Locate every leukocyte (white blood cell).
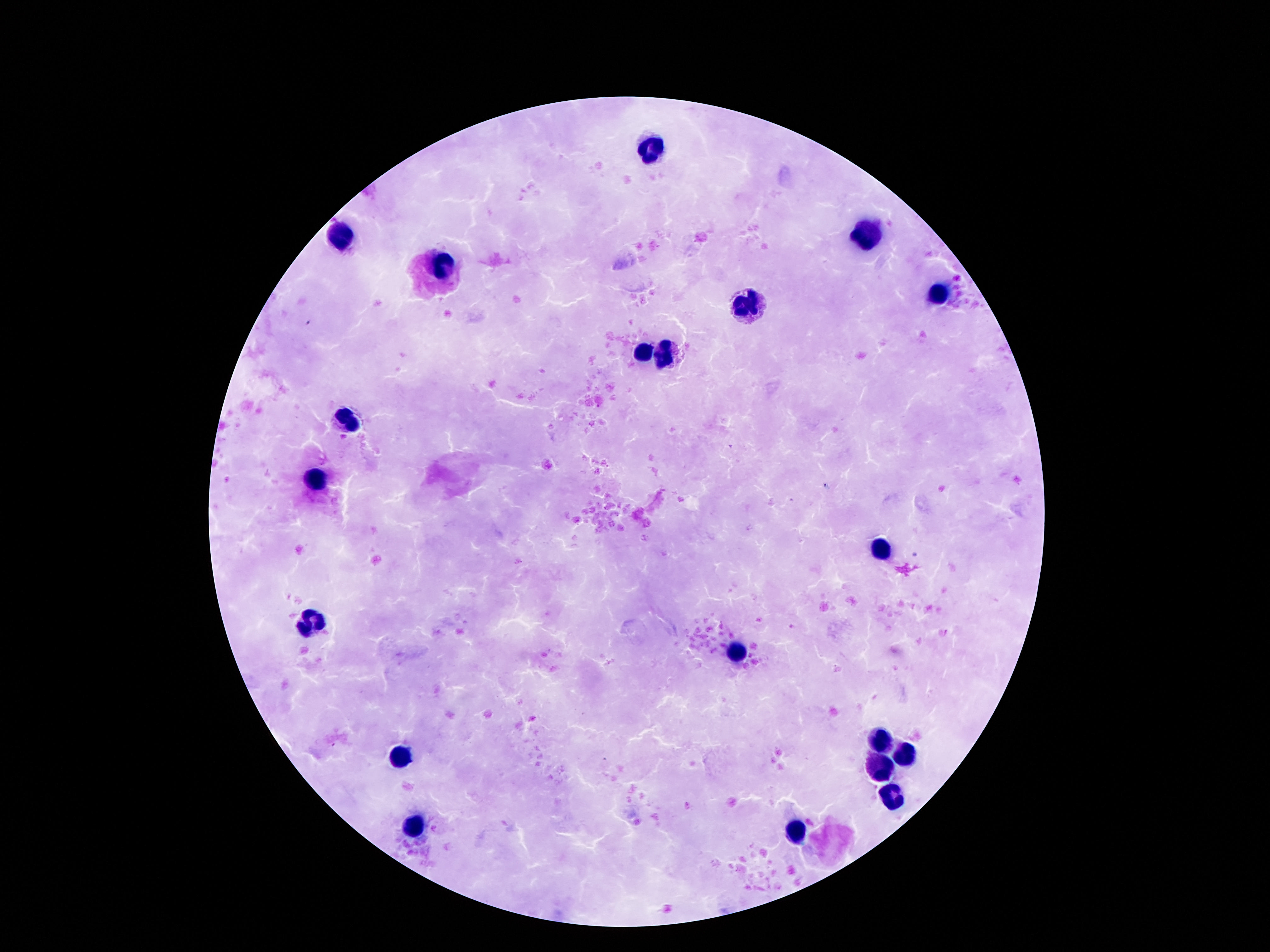
Approximate centers as {x, y} in pixels.
Leukocytes: {651, 149}, {864, 233}, {340, 235}, {446, 264}, {939, 295}, {746, 307}, {638, 354}, {667, 359}, {346, 418}, {315, 482}, {881, 549}, {313, 623}, {738, 652}, {879, 739}, {903, 754}, {404, 758}, {881, 770}, {888, 798}, {415, 828}, {799, 834}.

Summary:
  - Preparation: thick peripheral-blood smear
  - Capture: smartphone camera through the microscope eyepiece
  - Stain: Giemsa
  - Patient malaria status: negative
  - Magnification: 100x
  - Image size: 1270×952 pixels
  - Field of view: one from this slide